Comment on the morphology of the erythrocytes.
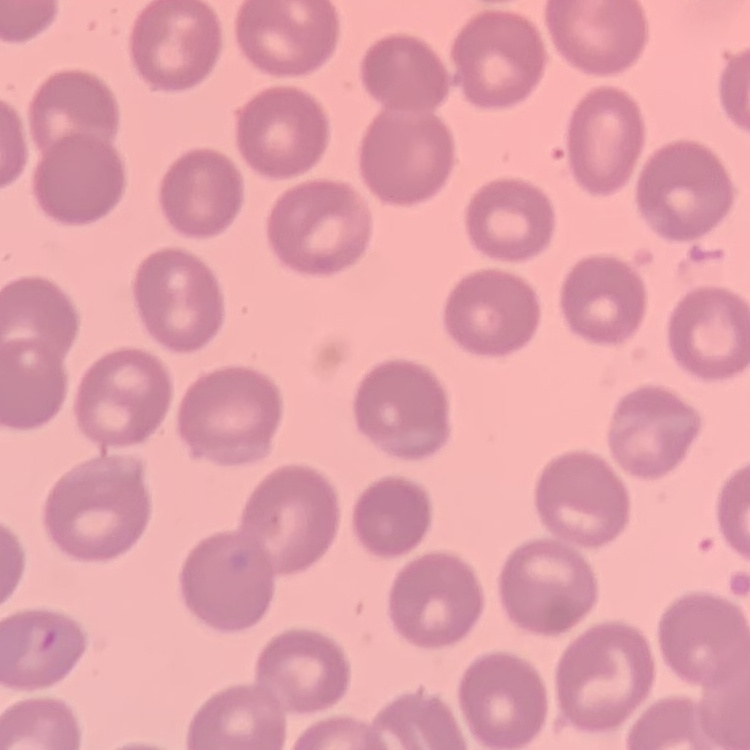

No rouleaux formation.

Summary:
  - Stain: Field's or Giemsa
  - Image type: one tile cut from a larger photomicrograph
  - Preparation: thin blood film